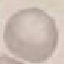
Summary:
  - Result: no malaria parasites seen
  - Image type: cell patch, automatically extracted from a larger field of view and resized to 64 × 64 pixels
  - Capture: smartphone through the microscope eyepiece
  - Preparation: thin smear
  - Stain: Giemsa